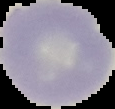

{
  "image_type": "segmented cell region with the area outside set to black",
  "malaria_status": "uninfected",
  "image_size": "115×109 pixels",
  "preparation": "thin blood smear"
}